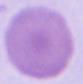
modality = micrograph
identification = red blood cell
magnification = 1000x